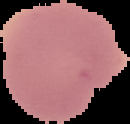 Result: no Plasmodium parasites seen. Image is 130×124 pixels. The area outside the segmented cell region is set to black. From a thin blood smear.